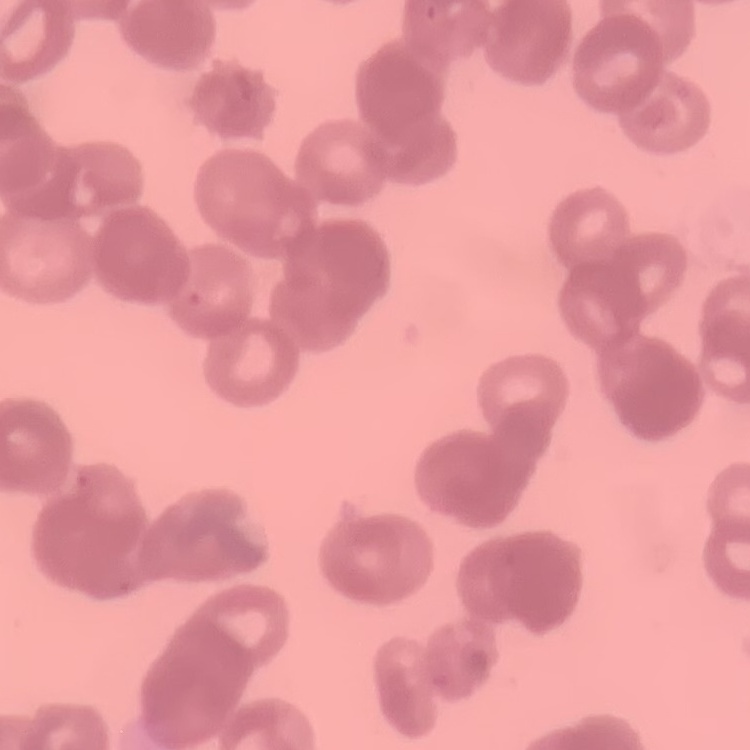

{
  "red_blood_cell_morphology": "rouleaux formation",
  "stain": "Field's or Giemsa",
  "preparation": "thin blood smear",
  "image_type": "one tile cut from a larger photomicrograph"
}